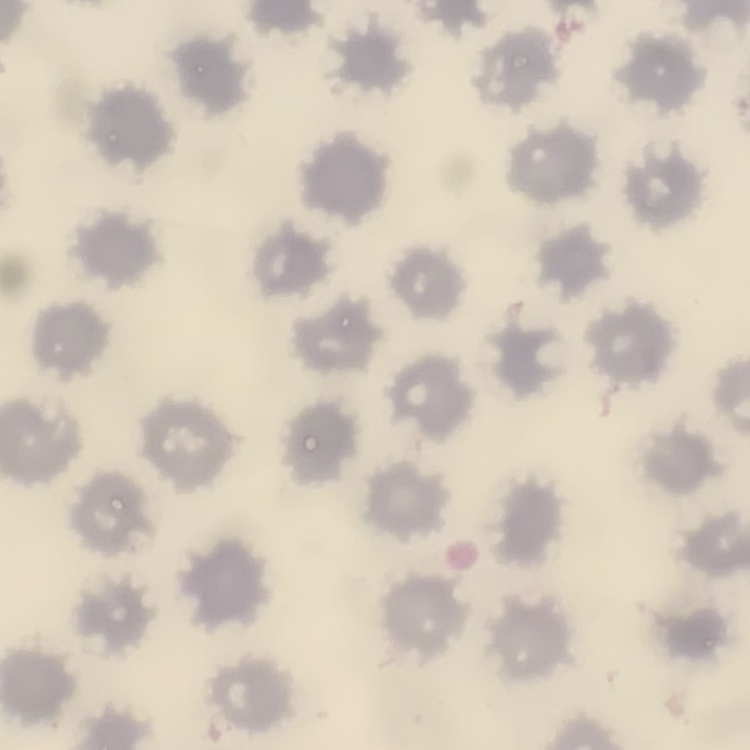 The erythrocytes show no rouleaux formation. Thin blood smear. Square crop of a larger photomicrograph. Stained with either Field's or Giemsa.